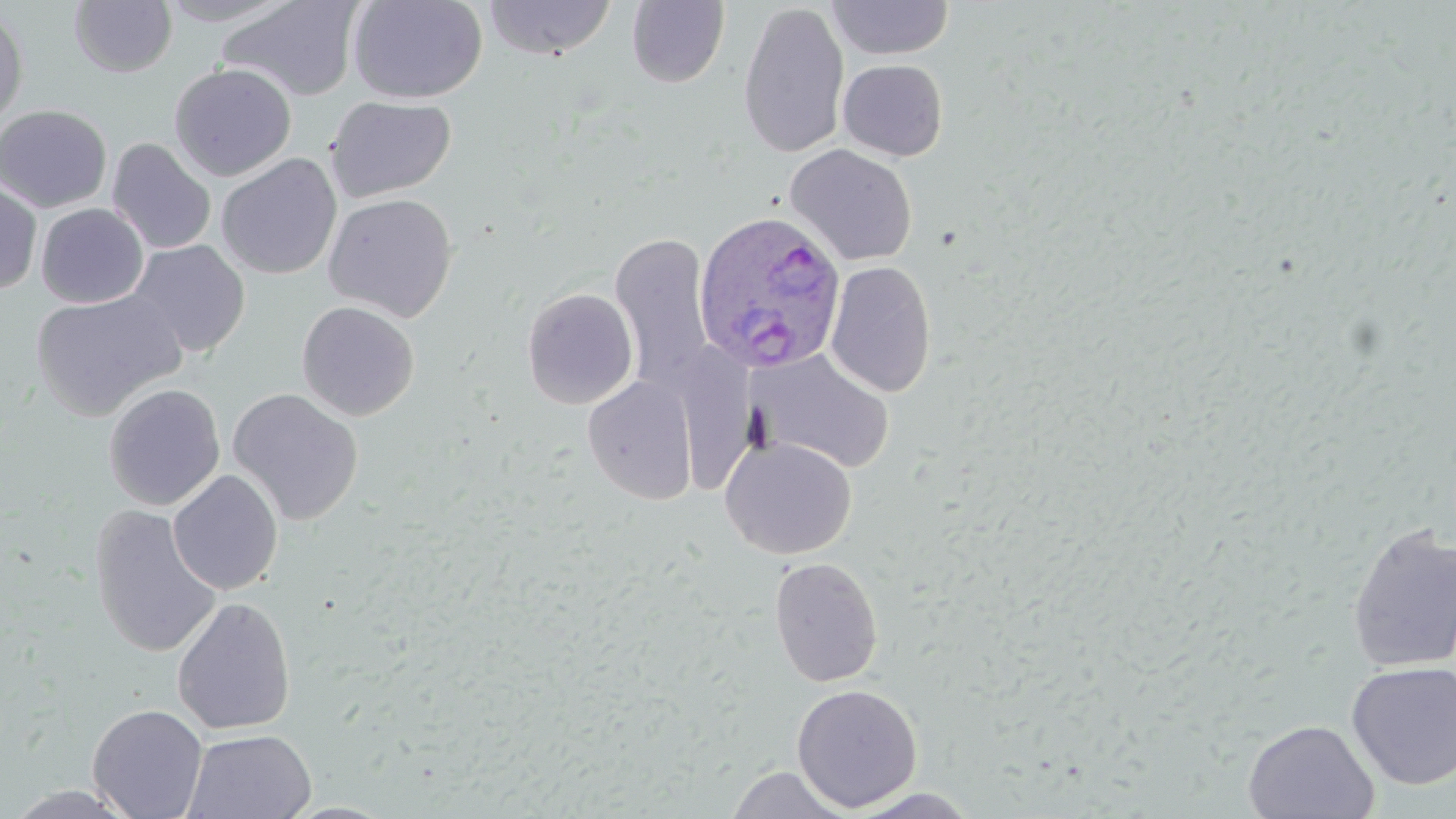

slide-level diagnosis = Plasmodium ovale
stain = May-Grünwald-Giemsa
magnification = 1000x
field of view = single
modality = optical microscopy
Plasmodium ovale-infected red blood cell locations = approximate bounding boxes as (x1, y1, x2, y2) in pixels: (694, 209, 851, 376)
image size = 1456×819 pixels
uninfected red blood cell locations = approximate bounding boxes as (x1, y1, x2, y2) in pixels: (156, 0, 297, 26), (218, 0, 365, 102), (348, 0, 488, 103), (485, 0, 617, 60), (826, 0, 954, 60), (69, 1, 178, 77), (626, 1, 729, 88), (737, 2, 850, 158), (0, 6, 29, 130), (838, 59, 948, 161), (169, 62, 297, 181), (325, 95, 456, 202), (0, 104, 112, 213), (107, 138, 216, 255), (784, 144, 918, 266), (216, 153, 342, 280), (0, 180, 43, 294), (323, 192, 458, 322), (36, 203, 149, 308), (610, 230, 715, 393), (128, 239, 250, 357), (825, 260, 937, 398), (521, 287, 638, 409), (31, 289, 186, 421), (297, 301, 420, 421), (681, 342, 763, 489), (750, 349, 896, 474), (582, 376, 698, 505), (103, 383, 225, 510), (226, 387, 364, 525), (719, 435, 857, 559), (168, 470, 283, 595), (88, 504, 223, 659), (1346, 523, 1456, 673), (768, 556, 883, 687), (172, 597, 296, 736), (1346, 660, 1456, 790), (791, 683, 923, 813), (87, 703, 208, 819), (1242, 719, 1380, 819), (183, 728, 317, 819), (725, 765, 852, 818), (3, 785, 142, 819), (845, 788, 984, 818)
preparation = thin blood smear